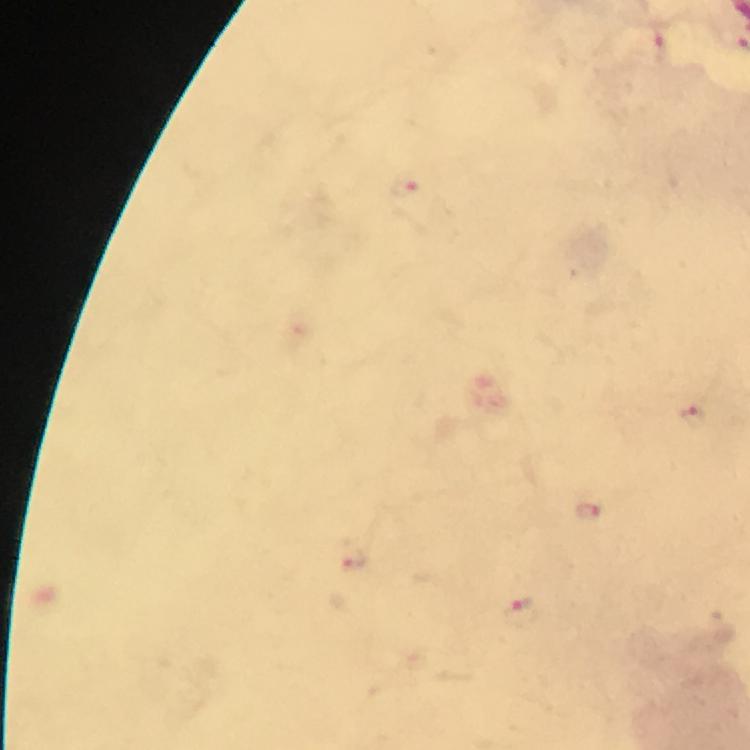
image_size: 750×750 pixels
context: from a diagnostic examination for malaria
stain: Giemsa
plasmodium_parasite_locations: 'approximate object centers, in pixels from the top-left corner: (x=663, y=46), (x=403, y=187), (x=696, y=414), (x=590, y=512), (x=352, y=554), (x=520, y=611)'
capture: smartphone photograph through a microscope
immersion_oil: used
preparation: thick smear
cropped_from: a single field of view
magnification: 100x